Name the parasite shown.
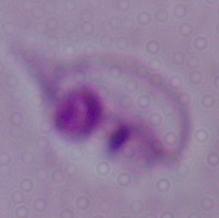
This is Leishmania.

{
  "modality": "micrograph",
  "magnification": "1000x"
}